Report the malaria status of this cell.
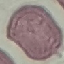

It is uninfected.

Cell patch, automatically extracted from a larger field of view and resized to 64 × 64 pixels. Photographed with a smartphone camera at the microscope eyepiece. Giemsa stain. Thin smear of blood.